State the blood parasite species.
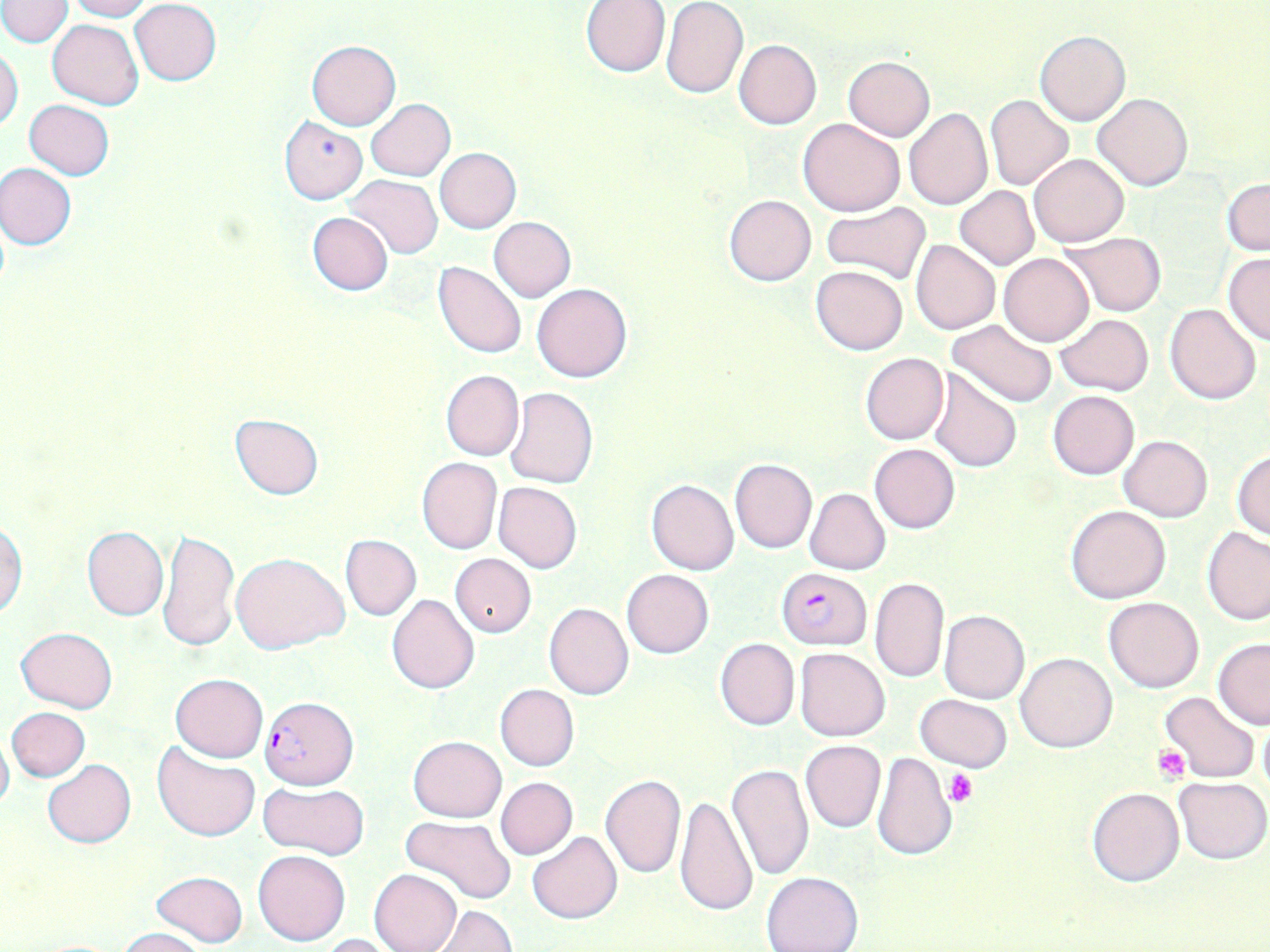

Plasmodium falciparum.

{
  "platelet_locations": "approximate bounding boxes as named x1/y1/x2/y2 corners in pixels: (x1=1152, y1=745, x2=1190, y2=783), (x1=947, y1=771, x2=978, y2=806)",
  "uninfected_red_blood_cell_locations": "approximate bounding boxes as named x1/y1/x2/y2 corners in pixels: (x1=63, y1=0, x2=152, y2=21), (x1=579, y1=0, x2=671, y2=76), (x1=0, y1=1, x2=73, y2=47), (x1=129, y1=1, x2=221, y2=86), (x1=661, y1=3, x2=749, y2=99), (x1=48, y1=18, x2=143, y2=110), (x1=1036, y1=30, x2=1130, y2=124), (x1=734, y1=39, x2=822, y2=129), (x1=306, y1=40, x2=400, y2=129), (x1=0, y1=48, x2=24, y2=132), (x1=843, y1=56, x2=934, y2=141), (x1=1093, y1=93, x2=1193, y2=191), (x1=985, y1=95, x2=1074, y2=190), (x1=24, y1=99, x2=114, y2=179), (x1=366, y1=99, x2=454, y2=181), (x1=903, y1=109, x2=992, y2=211), (x1=278, y1=115, x2=367, y2=205), (x1=798, y1=118, x2=906, y2=216), (x1=435, y1=147, x2=522, y2=233), (x1=1029, y1=153, x2=1129, y2=247), (x1=0, y1=163, x2=76, y2=250), (x1=344, y1=175, x2=443, y2=260), (x1=1223, y1=178, x2=1269, y2=256), (x1=954, y1=186, x2=1039, y2=269), (x1=724, y1=195, x2=816, y2=285), (x1=821, y1=202, x2=931, y2=285), (x1=307, y1=212, x2=394, y2=296), (x1=488, y1=216, x2=575, y2=301), (x1=1059, y1=232, x2=1164, y2=317), (x1=911, y1=240, x2=1000, y2=335), (x1=999, y1=253, x2=1094, y2=346), (x1=1222, y1=253, x2=1270, y2=345), (x1=434, y1=261, x2=527, y2=359), (x1=811, y1=265, x2=907, y2=355), (x1=532, y1=283, x2=632, y2=383), (x1=1165, y1=302, x2=1262, y2=404), (x1=1055, y1=313, x2=1153, y2=395), (x1=948, y1=319, x2=1058, y2=409), (x1=861, y1=352, x2=949, y2=445), (x1=440, y1=369, x2=524, y2=462), (x1=928, y1=369, x2=1022, y2=473), (x1=505, y1=387, x2=597, y2=488), (x1=1048, y1=389, x2=1139, y2=479), (x1=229, y1=411, x2=322, y2=501), (x1=1119, y1=435, x2=1212, y2=521), (x1=869, y1=444, x2=961, y2=534), (x1=1231, y1=450, x2=1270, y2=540), (x1=417, y1=458, x2=501, y2=553), (x1=730, y1=459, x2=816, y2=552), (x1=646, y1=479, x2=739, y2=575), (x1=493, y1=482, x2=582, y2=574), (x1=804, y1=488, x2=890, y2=575), (x1=1066, y1=504, x2=1171, y2=603), (x1=0, y1=517, x2=26, y2=619), (x1=82, y1=525, x2=169, y2=621), (x1=1201, y1=526, x2=1270, y2=624), (x1=158, y1=528, x2=240, y2=652), (x1=340, y1=533, x2=421, y2=621), (x1=231, y1=552, x2=349, y2=654), (x1=450, y1=553, x2=536, y2=637), (x1=622, y1=568, x2=713, y2=658), (x1=869, y1=576, x2=950, y2=684), (x1=386, y1=594, x2=479, y2=694), (x1=1103, y1=596, x2=1204, y2=692), (x1=544, y1=602, x2=634, y2=700), (x1=940, y1=611, x2=1029, y2=703), (x1=16, y1=626, x2=117, y2=713), (x1=715, y1=638, x2=799, y2=730), (x1=1213, y1=638, x2=1270, y2=730), (x1=795, y1=647, x2=891, y2=741), (x1=1016, y1=653, x2=1117, y2=753), (x1=170, y1=673, x2=267, y2=762), (x1=495, y1=684, x2=578, y2=771), (x1=1160, y1=689, x2=1260, y2=783), (x1=915, y1=694, x2=1012, y2=771), (x1=6, y1=707, x2=91, y2=781), (x1=1257, y1=710, x2=1270, y2=803), (x1=0, y1=728, x2=13, y2=818), (x1=409, y1=736, x2=506, y2=822), (x1=800, y1=740, x2=886, y2=833), (x1=153, y1=742, x2=259, y2=842), (x1=872, y1=751, x2=957, y2=859), (x1=43, y1=759, x2=136, y2=848), (x1=727, y1=763, x2=813, y2=880), (x1=599, y1=775, x2=686, y2=880), (x1=495, y1=777, x2=577, y2=860), (x1=1173, y1=777, x2=1269, y2=864), (x1=256, y1=781, x2=369, y2=859), (x1=1087, y1=787, x2=1185, y2=887), (x1=674, y1=794, x2=757, y2=918), (x1=400, y1=816, x2=516, y2=905), (x1=528, y1=831, x2=622, y2=924), (x1=253, y1=850, x2=351, y2=947), (x1=370, y1=869, x2=462, y2=952), (x1=151, y1=871, x2=249, y2=946), (x1=761, y1=872, x2=863, y2=952), (x1=430, y1=905, x2=516, y2=952), (x1=117, y1=928, x2=207, y2=952), (x1=319, y1=933, x2=400, y2=952)",
  "magnification": "1000x",
  "stain": "May-Grünwald-Giemsa",
  "preparation": "thin blood film",
  "modality": "light microscopy",
  "field_of_view": "single",
  "image_size": "1270×952 pixels",
  "plasmodium_falciparum_infected_red_blood_cell_locations": "approximate bounding boxes as named x1/y1/x2/y2 corners in pixels: (x1=776, y1=567, x2=872, y2=650), (x1=259, y1=695, x2=359, y2=788)"
}